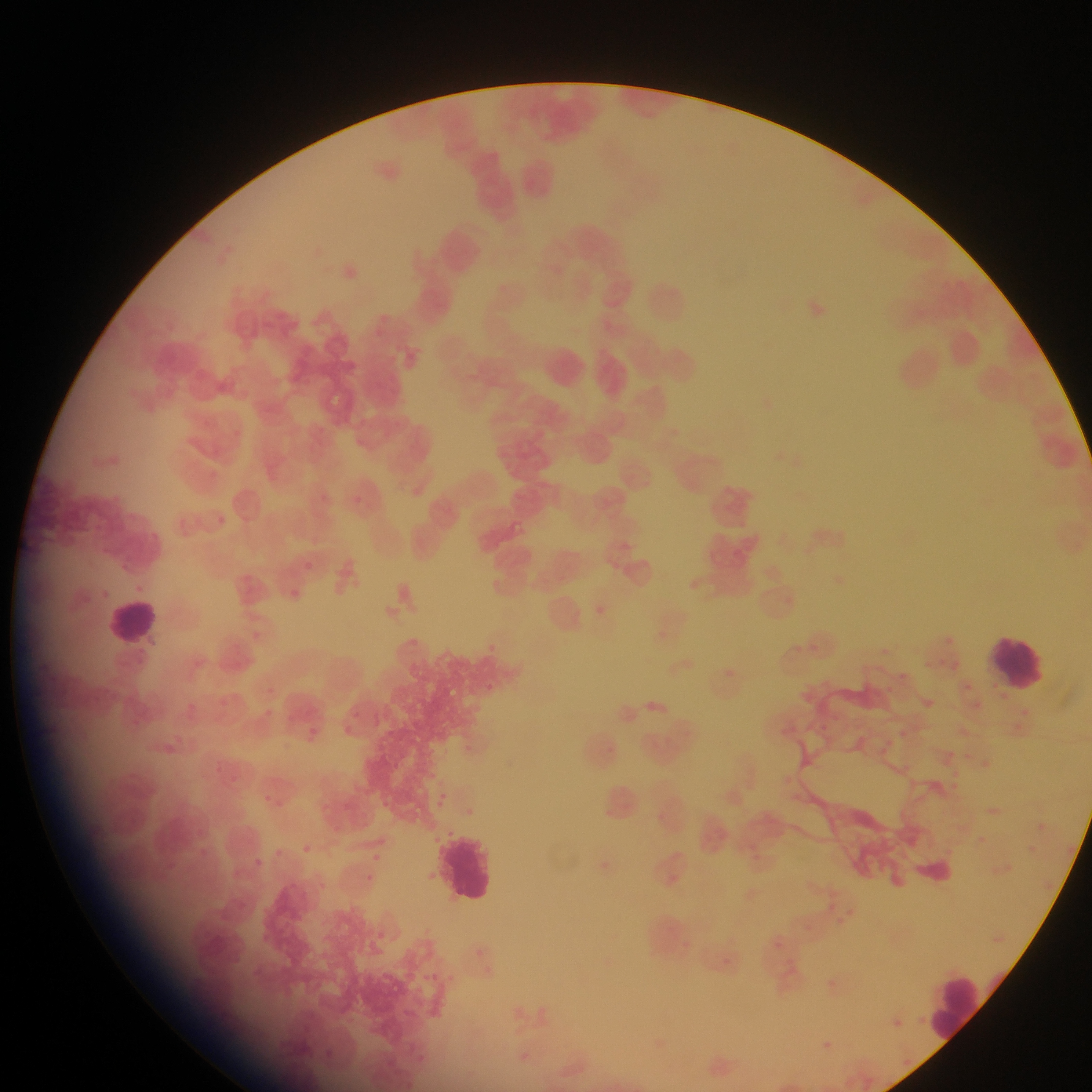

Approximate bounding boxes as [left, top, right, bottom] in pixels.
Summary:
  - Leukocyte locations: [104, 594, 163, 650], [989, 631, 1052, 694], [437, 823, 502, 907], [932, 972, 991, 1048]
  - Malaria parasite locations: [352, 494, 361, 503], [217, 515, 226, 523], [301, 561, 313, 572], [290, 588, 301, 599], [596, 603, 608, 617], [657, 627, 670, 637], [946, 628, 966, 657], [487, 641, 508, 663], [793, 641, 808, 657], [877, 645, 887, 656], [870, 660, 888, 676], [896, 665, 912, 688], [723, 668, 738, 679], [958, 681, 969, 692], [483, 682, 497, 693], [877, 689, 893, 697], [919, 693, 938, 709], [833, 709, 839, 718], [365, 711, 386, 729], [341, 721, 352, 737], [305, 722, 322, 738], [815, 722, 828, 738], [898, 727, 912, 741], [947, 744, 960, 757], [978, 757, 993, 770], [948, 767, 957, 774], [229, 775, 238, 783], [951, 781, 960, 790], [437, 791, 450, 812], [990, 803, 1004, 820], [1031, 818, 1052, 833], [971, 831, 989, 851], [1023, 836, 1039, 857], [296, 841, 309, 856], [368, 849, 382, 864], [1004, 858, 1018, 873], [363, 876, 370, 886], [775, 937, 791, 959], [468, 946, 482, 961], [727, 954, 748, 975], [441, 968, 455, 986], [421, 971, 434, 983], [416, 989, 420, 998], [914, 1011, 925, 1021], [891, 1017, 905, 1028], [825, 1034, 838, 1049], [901, 1053, 916, 1062]
  - Preparation: thin blood film
  - Image size: 1092×1092 pixels
  - Field of view: single
  - Country: Ghana
  - Capture: mobile-phone photograph through a microscope